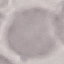

Result: negative for malaria parasites. Giemsa stain. Cell patch, automatically extracted from a larger field of view and resized to 64 × 64 pixels. Thin blood film. Photographed with a smartphone camera at the microscope eyepiece.